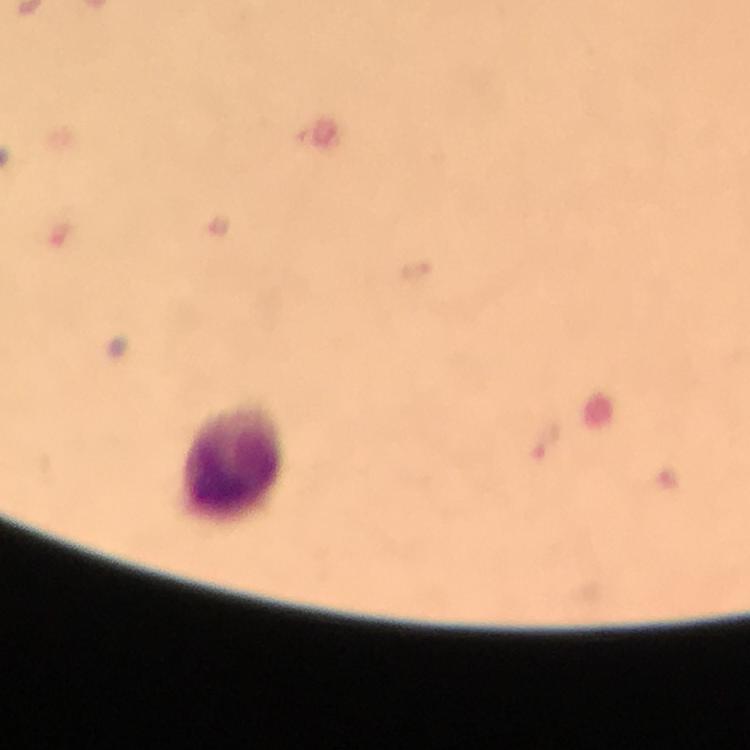
{
  "preparation": "thick blood film",
  "context": "from a diagnostic examination for malaria",
  "image_size": "750×750 pixels",
  "magnification": "100x",
  "capture": "smartphone photograph through a microscope",
  "plasmodium_parasite_locations": "approximate centers as [x, y] in pixels: [544, 441]",
  "immersion_oil": "applied",
  "leukocyte_locations": "approximate centers as [x, y] in pixels: [231, 463]",
  "stain": "Giemsa",
  "cropped_from": "a single field of view"
}